Locate every blood parasite and identify its species.
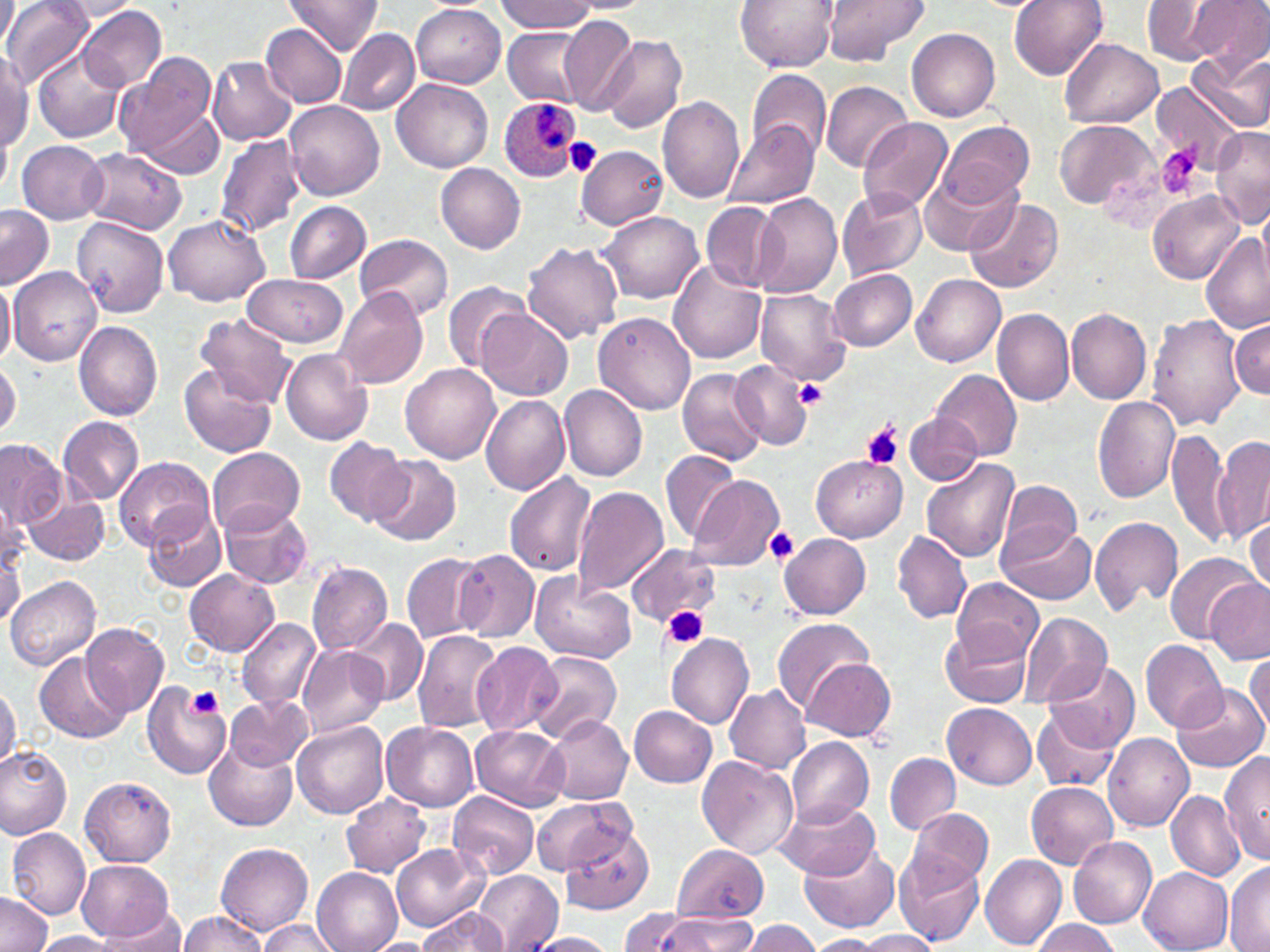

Approximate bounding boxes as (x1, y1, x2, y2) in pixels.
Plasmodium ovale-infected red blood cells: (497, 95, 583, 181).
No Plasmodium falciparum, Plasmodium malariae, Plasmodium vivax, Babesia divergens, or Trypanosoma brucei observed.

Summary:
  - Platelet locations: (564, 137, 603, 176), (1156, 145, 1204, 199), (795, 377, 829, 409), (861, 422, 903, 468), (764, 526, 801, 566), (663, 606, 707, 649), (187, 685, 222, 720)
  - Uninfected red blood cell locations: (0, 0, 17, 53), (284, 0, 383, 54), (735, 0, 838, 71), (821, 0, 929, 65), (1009, 0, 1109, 80), (1188, 0, 1270, 73), (2, 1, 94, 89), (1140, 1, 1235, 65), (57, 2, 145, 20), (495, 2, 597, 34), (77, 4, 167, 95), (412, 5, 506, 87), (558, 15, 639, 115), (262, 24, 346, 107), (337, 28, 418, 116), (907, 28, 1001, 121), (504, 29, 588, 104), (599, 35, 687, 133), (1060, 39, 1163, 129), (1187, 49, 1270, 135), (0, 50, 32, 154), (33, 50, 124, 144), (114, 52, 218, 166), (206, 55, 296, 144), (747, 68, 831, 160), (392, 77, 493, 173), (821, 80, 912, 172), (1152, 83, 1246, 171), (657, 95, 746, 203), (285, 101, 385, 202), (141, 108, 224, 178), (858, 117, 952, 215), (1054, 119, 1157, 210), (936, 121, 1034, 207), (726, 122, 818, 209), (0, 127, 11, 198), (1210, 127, 1270, 229), (214, 133, 307, 239), (17, 140, 108, 225), (576, 144, 670, 230), (78, 148, 188, 236), (435, 163, 526, 253), (920, 165, 1020, 258), (837, 189, 926, 281), (1148, 189, 1244, 286), (752, 193, 843, 299), (964, 197, 1063, 294), (283, 200, 371, 284), (703, 202, 782, 291), (0, 206, 55, 287), (599, 211, 704, 304), (164, 214, 270, 306), (74, 217, 169, 318), (1199, 231, 1268, 333), (356, 234, 452, 321), (522, 242, 623, 344), (669, 261, 769, 363), (9, 266, 101, 368), (827, 267, 916, 351), (242, 272, 348, 347), (912, 275, 1005, 368), (0, 276, 14, 370), (441, 279, 530, 373), (333, 287, 429, 391), (755, 287, 852, 386), (476, 308, 572, 399), (1065, 308, 1151, 404), (993, 309, 1074, 406), (594, 311, 695, 414), (196, 312, 296, 408), (1146, 314, 1245, 431), (1231, 319, 1269, 400), (73, 321, 163, 420), (281, 348, 371, 445), (0, 361, 21, 440), (400, 362, 501, 465), (729, 362, 814, 451), (179, 364, 276, 458), (678, 368, 767, 466), (931, 369, 1021, 464), (559, 384, 647, 481), (481, 395, 571, 496), (1092, 396, 1180, 502), (904, 411, 982, 485), (58, 416, 143, 504), (1167, 429, 1233, 548), (1212, 435, 1269, 544), (323, 437, 412, 524), (0, 440, 66, 527), (207, 447, 305, 536), (661, 450, 742, 546), (368, 454, 462, 546), (812, 456, 906, 541), (115, 457, 213, 550), (920, 458, 1020, 565), (502, 472, 597, 579), (689, 475, 786, 572), (998, 480, 1083, 557), (573, 485, 669, 597), (23, 493, 110, 566), (0, 496, 27, 576), (220, 503, 312, 589), (143, 507, 225, 594), (1091, 516, 1184, 615), (1246, 517, 1269, 595), (997, 521, 1096, 605), (892, 531, 973, 625), (778, 532, 871, 617), (1, 537, 25, 623), (626, 542, 720, 626), (453, 549, 541, 641), (1164, 549, 1262, 646), (401, 552, 486, 643), (307, 561, 393, 656), (185, 570, 279, 656), (530, 574, 635, 664), (6, 575, 100, 670), (951, 577, 1044, 662), (1202, 578, 1270, 665), (1019, 612, 1114, 709), (236, 617, 321, 711), (771, 617, 875, 716), (348, 619, 427, 705), (79, 621, 168, 718), (941, 623, 1031, 707), (411, 630, 504, 734), (666, 632, 754, 727), (1140, 639, 1228, 735), (471, 642, 563, 738), (298, 644, 388, 740), (35, 651, 129, 743), (527, 652, 622, 744), (1246, 652, 1269, 735), (803, 657, 896, 742), (1042, 658, 1140, 754), (723, 683, 810, 774), (0, 684, 20, 773), (143, 684, 230, 780), (1174, 685, 1267, 772), (225, 695, 312, 770), (943, 702, 1038, 788), (629, 705, 717, 786), (1033, 708, 1119, 793), (542, 715, 634, 805), (292, 721, 388, 818), (381, 722, 478, 811), (470, 725, 569, 811), (1104, 733, 1194, 832), (786, 737, 874, 829), (202, 738, 297, 831), (0, 745, 73, 838), (1218, 752, 1269, 864), (886, 753, 960, 834), (697, 755, 799, 858), (80, 776, 176, 867), (1026, 782, 1118, 869), (1165, 790, 1245, 881), (449, 792, 540, 879), (340, 795, 432, 877), (530, 795, 634, 877), (775, 798, 879, 881), (908, 807, 995, 890), (561, 823, 655, 913), (8, 829, 91, 919), (1070, 836, 1157, 928), (798, 840, 900, 934), (216, 842, 313, 934), (391, 843, 487, 931), (672, 843, 769, 922), (895, 849, 985, 945), (979, 852, 1066, 950), (76, 859, 173, 942), (1224, 864, 1270, 952), (1140, 867, 1233, 952), (312, 868, 402, 952), (473, 870, 562, 950), (0, 891, 54, 952), (95, 907, 187, 950), (622, 907, 699, 952), (417, 908, 508, 950), (176, 910, 268, 952), (652, 915, 761, 951), (257, 919, 340, 952), (742, 919, 823, 952), (1029, 919, 1121, 952), (853, 929, 945, 951), (31, 931, 123, 951), (524, 932, 618, 952), (806, 935, 884, 951), (370, 940, 431, 952)
  - Slide-level diagnosis: Plasmodium ovale
  - Image size: 1270×952 pixels
  - Modality: light microscopy
  - Magnification: 1000x
  - Field of view: single
  - Preparation: thin blood film
  - Stain: May-Grünwald-Giemsa